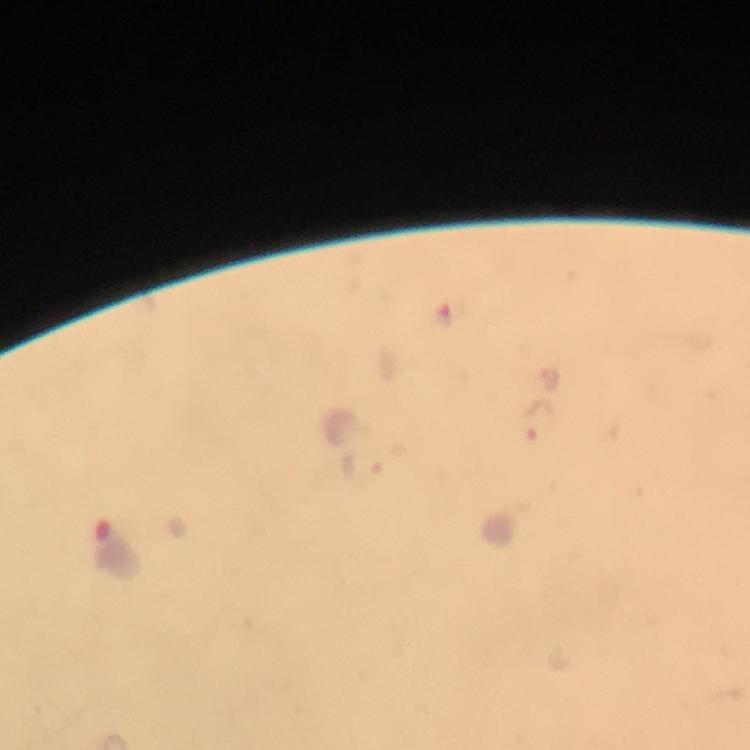 Approximate object centers, in pixels from the top-left corner. Plasmodium parasite locations: (x=448, y=312), (x=551, y=378), (x=537, y=422). Immersion oil applied. Giemsa-stained preparation. Image is 750×750 pixels. From a diagnostic examination for malaria. Thick blood film. 100x magnification. Photographed through the microscope with a smartphone camera. Cropped region of a single field of view.